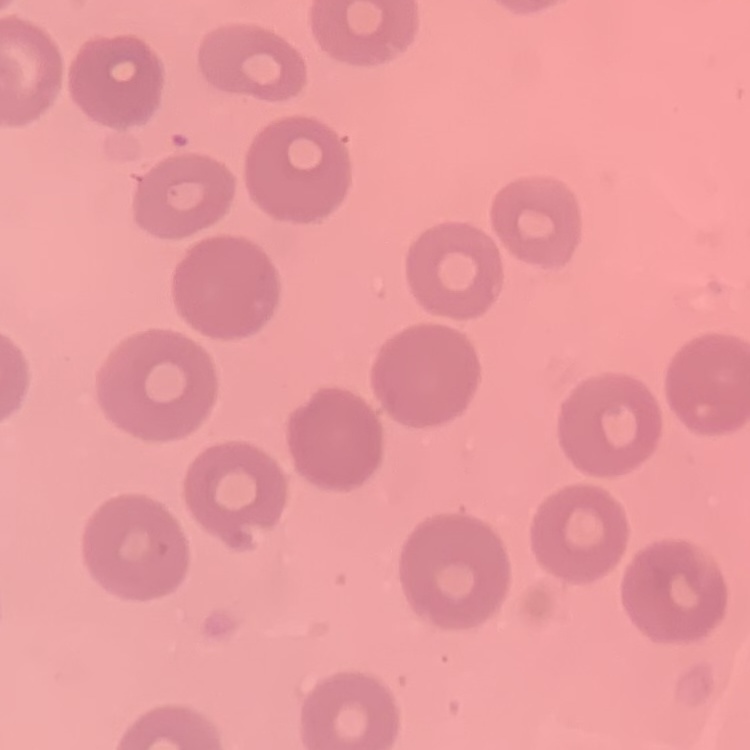
The erythrocytes exhibit no rouleaux formation. Thin blood smear. Field's or Giemsa stain. One tile cut from a larger photomicrograph.